Assess this cell for malaria.
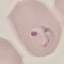

It is parasitized.

Acquired by smartphone through the microscope eyepiece. Automatically extracted cell patch, resized to 64 × 64 pixels. Giemsa-stained preparation. Thin blood film.